Classify this cell by malaria status.
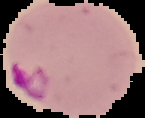
Parasitized.

Summary:
  - Preparation: thin blood film
  - Image size: 145×118 pixels
  - Image type: cell region segmented out of the field of view; surrounding area masked to black